Describe the morphology of the red blood cells.
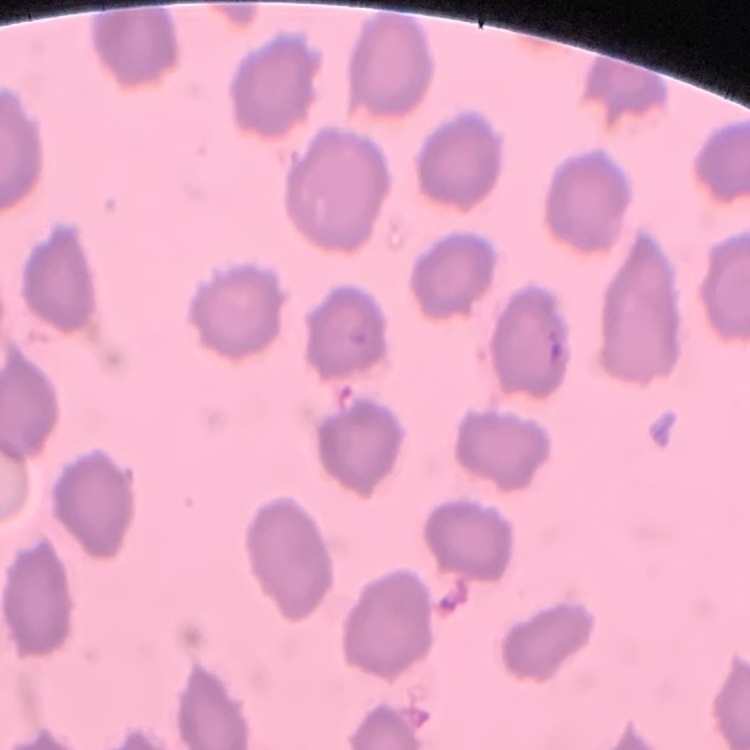

They show no rouleaux formation.

stain = Field's or Giemsa
preparation = thin blood film
image type = one tile cut from a larger photomicrograph